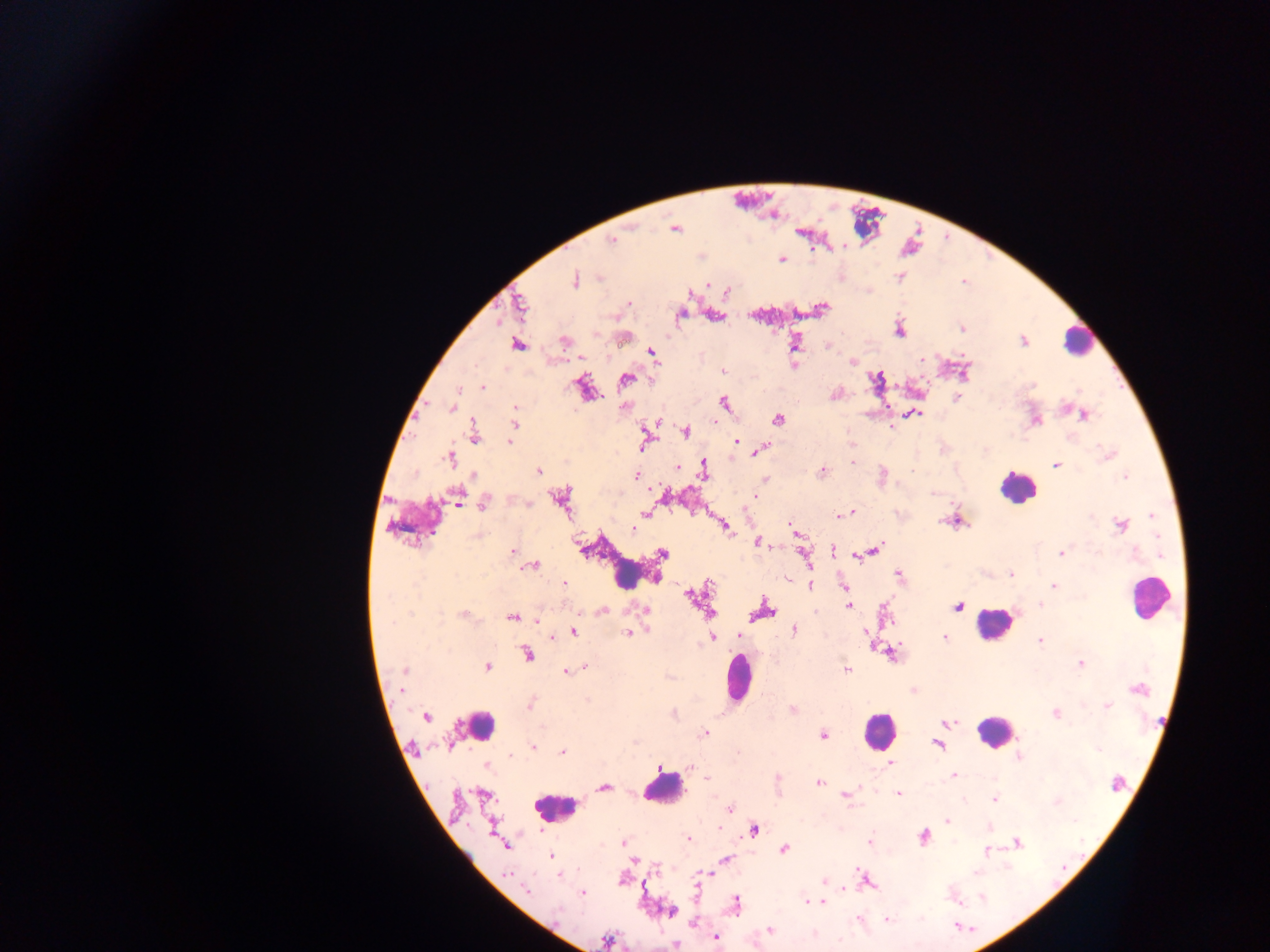
malaria_parasite_locations: 'approximate centers as (x, y) in pixels: (675, 229), (611, 240), (781, 259), (899, 277), (601, 278), (574, 280), (629, 303), (520, 304), (822, 309), (680, 315), (962, 328), (900, 331), (564, 341), (1023, 341), (518, 345), (652, 353), (923, 359), (853, 362), (794, 365), (723, 372), (878, 378), (626, 379), (483, 387), (957, 397), (724, 403), (626, 406), (516, 407), (451, 408), (914, 413), (1084, 416), (777, 420), (1036, 420), (514, 423), (657, 423), (686, 432), (474, 434), (644, 441), (511, 442), (736, 442), (760, 451), (1108, 454), (449, 458), (852, 462), (1056, 465), (677, 467), (538, 470), (704, 470), (823, 471), (883, 471), (474, 476), (636, 476), (1126, 476), (765, 480), (932, 493), (457, 497), (756, 497), (561, 498), (484, 504), (526, 504), (849, 513), (646, 514), (840, 515), (1152, 516), (953, 521), (790, 525), (1121, 525), (724, 526), (633, 530), (759, 542), (834, 550), (874, 550), (513, 551), (866, 552), (1061, 553), (662, 554), (805, 557), (534, 565), (1011, 574), (898, 575), (656, 577), (563, 585), (810, 585), (1054, 585), (844, 588), (692, 596), (1040, 604), (848, 606), (958, 606), (646, 610), (602, 611), (765, 611), (709, 612), (463, 614), (511, 618), (794, 630), (573, 632), (628, 633), (865, 633), (738, 636), (945, 637), (713, 638), (1040, 640), (527, 654), (1081, 663), (487, 666), (583, 667), (847, 669), (405, 671), (567, 672), (1139, 688), (402, 690), (588, 700), (530, 704), (1108, 706), (792, 709), (1055, 714), (427, 716), (949, 722), (704, 733), (824, 735), (938, 745), (532, 747), (1098, 750), (563, 751), (511, 756), (1019, 756), (891, 763), (487, 766), (660, 768), (954, 775), (707, 778), (778, 780), (819, 783), (1116, 783), (604, 787), (846, 794), (898, 794), (995, 799), (1058, 801), (729, 808), (947, 820), (989, 827), (754, 830), (924, 837), (689, 839), (623, 842), (870, 842), (1018, 843), (505, 846), (784, 849), (987, 851), (550, 856), (725, 860), (977, 872), (560, 874), (708, 874), (507, 875), (824, 881), (868, 883), (526, 892), (583, 894), (982, 897), (809, 902), (818, 903), (736, 904), (557, 911), (671, 912), (858, 919), (887, 920), (770, 930), (716, 938), (607, 940), (676, 945)'
capture: mobile-phone photograph through a microscope
country: Ghana
image_size: 1270×952 pixels
preparation: thick blood film
leukocyte_locations: 'approximate centers as (x, y) in pixels: (1077, 340), (1018, 487), (627, 569), (1147, 598), (992, 624), (739, 678), (479, 725), (877, 731), (994, 731), (663, 790), (555, 808)'
field_of_view: single